Classify this cell by malaria status.
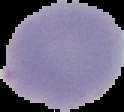
It is uninfected.

Image is 124×112 pixels. Segmented cell region on a black background. From a thin blood smear.